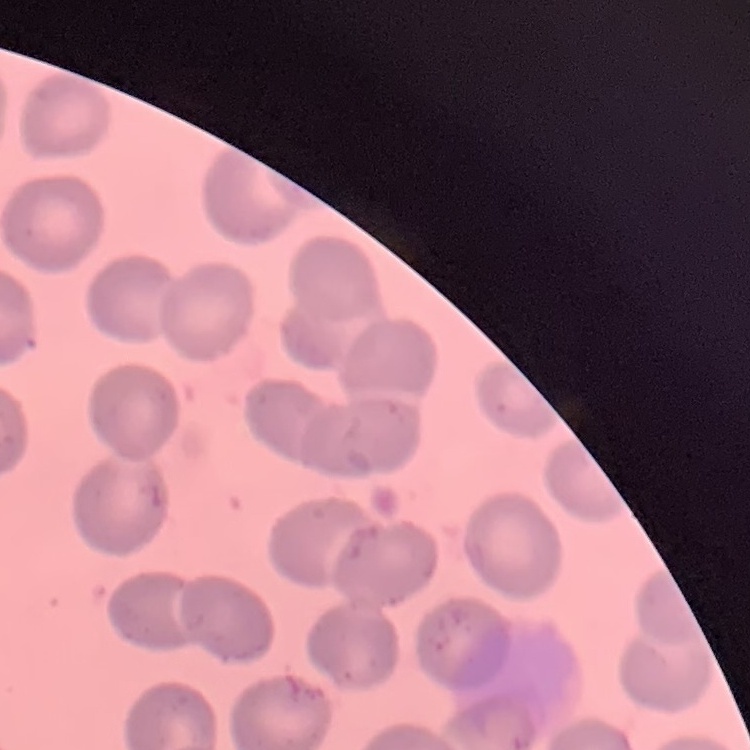

erythrocyte morphology = no rouleaux formation
preparation = thin blood film
stain = Field's or Giemsa
image type = one tile cut from a larger photomicrograph